State which cell type is depicted.
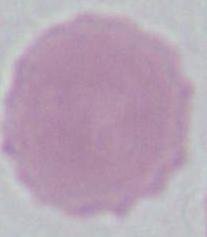
An erythrocyte.

Summary:
  - Modality: photomicrograph
  - Magnification: 1000x